Locate every blood parasite and identify its species.
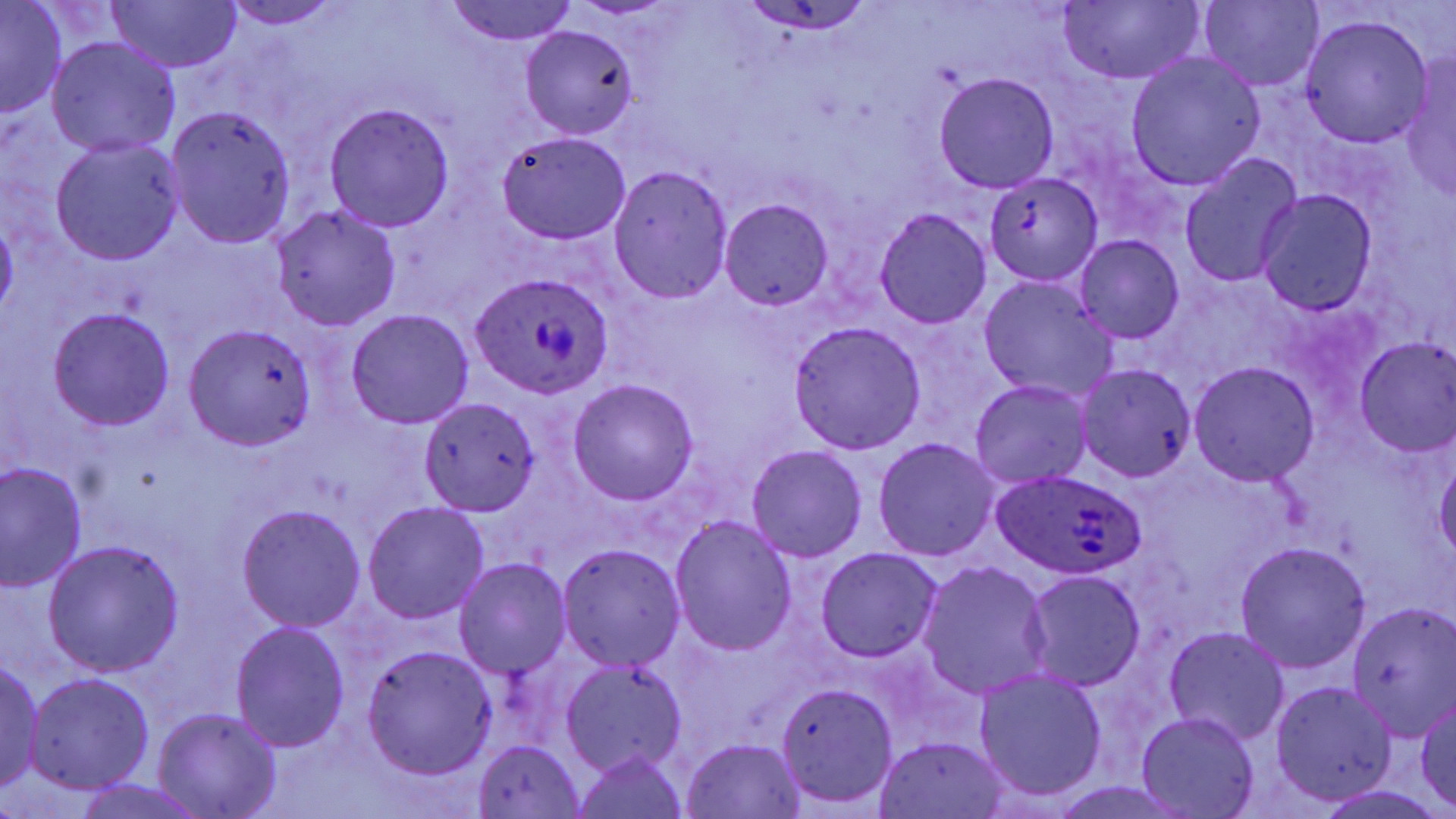
Approximate bounding boxes as [x1, y1, x2, y2] in pixels.
Plasmodium ovale-infected red blood cells: [471, 273, 609, 398], [991, 468, 1150, 581].
No Plasmodium falciparum, Plasmodium malariae, Plasmodium vivax, Babesia divergens, or Trypanosoma brucei observed.

Uninfected red blood cell locations: [1060, 0, 1206, 85], [111, 1, 240, 72], [218, 1, 347, 29], [441, 1, 577, 45], [1198, 1, 1324, 90], [0, 3, 66, 116], [742, 3, 873, 37], [1300, 14, 1435, 147], [520, 26, 638, 137], [46, 35, 181, 158], [1125, 53, 1265, 190], [1402, 57, 1456, 203], [934, 73, 1060, 193], [324, 102, 455, 232], [163, 105, 297, 248], [496, 131, 633, 244], [51, 137, 185, 265], [1179, 154, 1302, 290], [610, 166, 732, 303], [984, 174, 1103, 285], [1257, 192, 1378, 315], [722, 198, 833, 309], [271, 206, 401, 331], [876, 209, 991, 328], [0, 217, 18, 318], [1076, 235, 1184, 344], [979, 278, 1116, 402], [48, 306, 175, 431], [344, 308, 474, 429], [788, 320, 928, 451], [186, 323, 317, 450], [1353, 337, 1456, 454], [1189, 361, 1320, 486], [1075, 362, 1196, 481], [567, 378, 699, 505], [970, 380, 1091, 489], [419, 397, 540, 517], [873, 437, 999, 562], [747, 445, 867, 563], [1434, 457, 1456, 562], [0, 463, 87, 591], [362, 500, 491, 625], [235, 504, 366, 632], [669, 516, 797, 657], [43, 540, 184, 676], [1234, 542, 1370, 672], [557, 544, 686, 671], [815, 547, 941, 662], [454, 558, 572, 679], [919, 562, 1054, 699], [1023, 570, 1147, 690], [1344, 605, 1456, 739], [229, 621, 351, 753], [1164, 626, 1292, 746], [360, 644, 497, 779], [0, 658, 46, 793], [560, 661, 686, 777], [974, 668, 1108, 804], [25, 673, 154, 795], [1270, 680, 1399, 806], [775, 683, 900, 810], [1414, 695, 1456, 811], [153, 707, 282, 819], [1136, 712, 1259, 818], [874, 735, 1009, 818], [681, 738, 808, 818], [474, 739, 586, 818], [570, 749, 692, 819], [74, 779, 207, 819], [1048, 782, 1195, 818]. Slide-level diagnosis: Plasmodium ovale. May-Grünwald-Giemsa stain. Single field of view. Thin blood smear. Captured at 1000x magnification. Optical microscopy. Image is 1456×819 pixels.